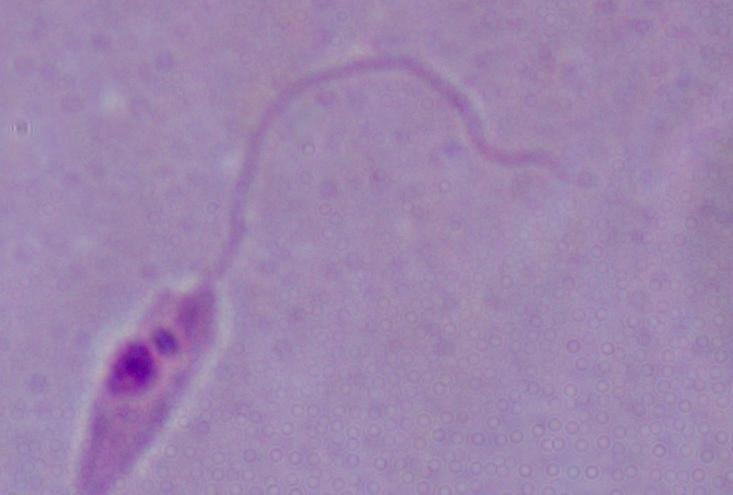

{
  "magnification": "1000x",
  "modality": "photomicrograph",
  "identification": "Leishmania"
}